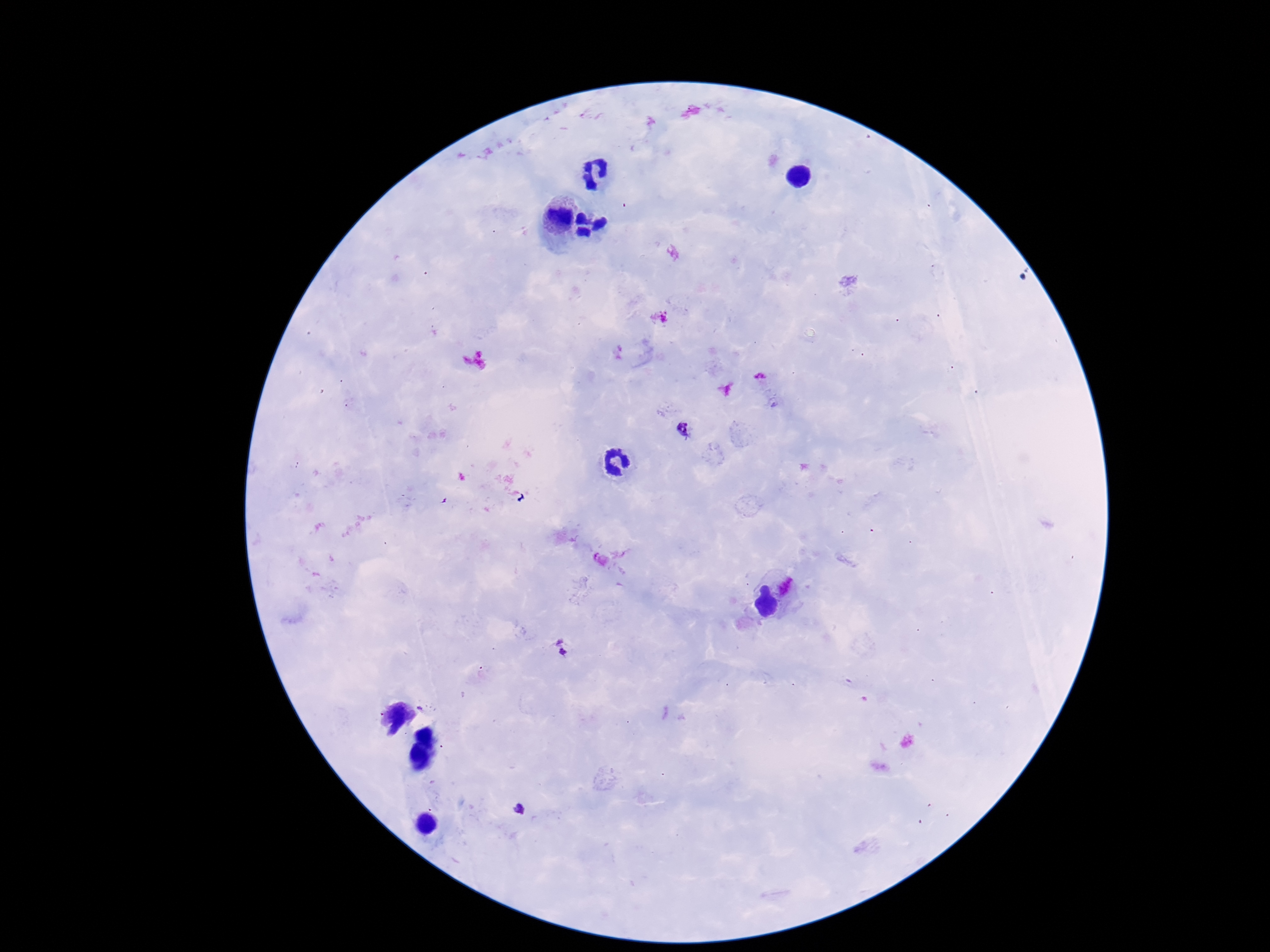
Approximate centers as [x, y] in pixels.
Summary:
  - Plasmodium parasite locations: [684, 429], [563, 651], [519, 809]
  - Stain: Giemsa
  - Field of view: single
  - Magnification: 100x
  - Capture: smartphone camera through the microscope eyepiece
  - Preparation: thick peripheral-blood smear
  - Image size: 1270×952 pixels
  - Patient malaria status: positive